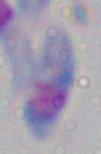 Captured at 1000x magnification. Toxoplasma gondii is shown. Photomicrograph.